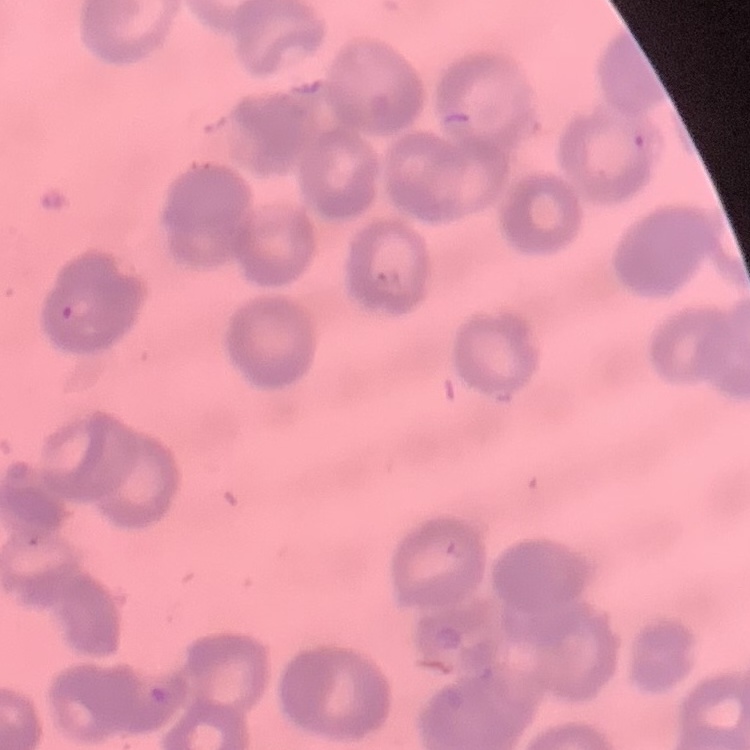
red blood cell morphology = rouleaux formation
preparation = thin blood smear
image type = square crop of a larger photomicrograph
stain = Field's or Giemsa